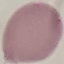
Result: negative for malaria parasites. Cell patch, automatically extracted from a larger field of view and resized to 64 × 64 pixels. Giemsa stain. Thin blood smear. Photographed with a smartphone camera at the microscope eyepiece.